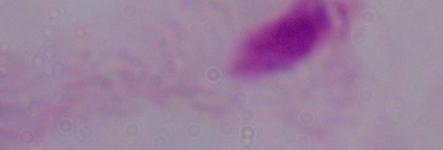
Summary:
  - Identification: trichomonad
  - Magnification: 1000x
  - Modality: photomicrograph